State which parasite is depicted.
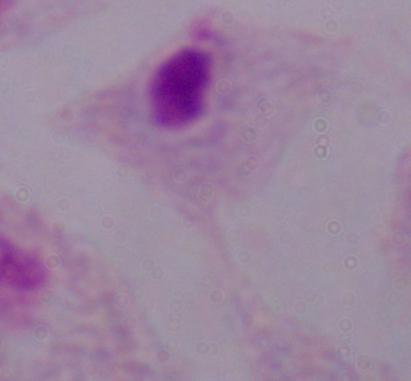

This is a trichomonad.

modality = photomicrograph
magnification = 1000x